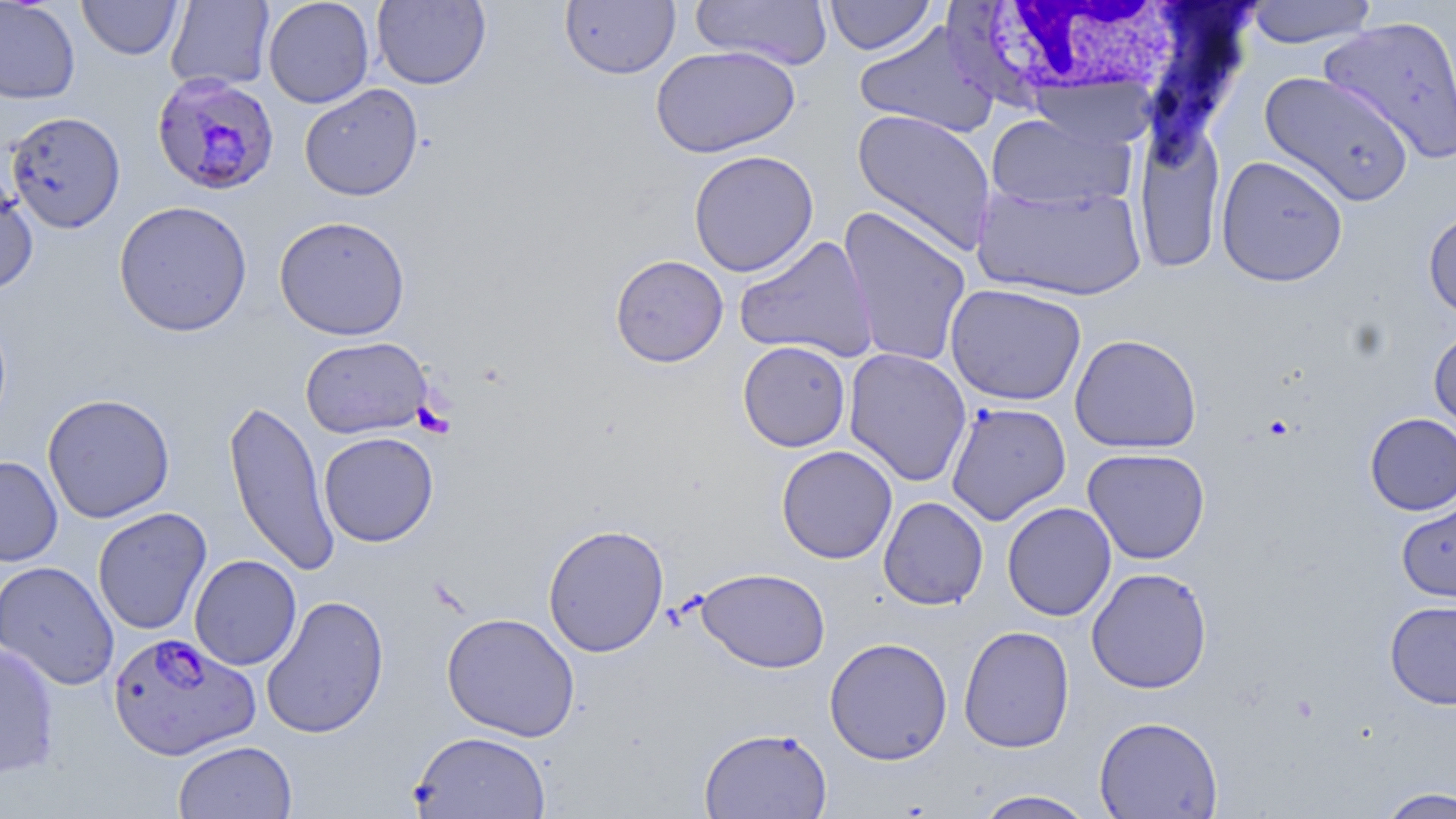
Summary:
  - Coordinate format: approximate bounding boxes as (x1, y1, x2, y2) in pixels
  - White blood cell locations: (949, 1, 1191, 107)
  - Plasmodium falciparum-infected red blood cell locations: (151, 72, 280, 196), (107, 631, 260, 761)
  - Platelet locations: (412, 403, 454, 437)
  - Uninfected red blood cell locations: (77, 0, 183, 60), (263, 0, 375, 108), (560, 0, 680, 80), (690, 0, 832, 70), (823, 0, 938, 56), (0, 1, 81, 104), (165, 1, 275, 92), (372, 1, 491, 89), (1244, 1, 1378, 48), (1319, 15, 1456, 162), (853, 20, 1000, 140), (650, 45, 801, 158), (1258, 71, 1416, 207), (299, 83, 423, 201), (851, 109, 997, 256), (5, 111, 125, 233), (985, 111, 1136, 212), (1134, 122, 1226, 275), (688, 150, 819, 277), (1216, 154, 1349, 287), (0, 171, 39, 296), (972, 181, 1148, 302), (113, 200, 253, 337), (838, 206, 973, 368), (1423, 208, 1456, 323), (274, 215, 411, 341), (734, 234, 879, 363), (609, 254, 729, 368), (944, 283, 1087, 406), (1429, 327, 1456, 440), (1069, 334, 1202, 454), (300, 336, 433, 439), (737, 340, 851, 452), (843, 347, 972, 487), (42, 393, 175, 523), (222, 397, 340, 577), (945, 401, 1072, 525), (1365, 412, 1456, 515), (318, 431, 438, 547), (776, 445, 897, 564), (1082, 447, 1210, 564), (0, 455, 63, 567), (1396, 496, 1456, 603), (878, 497, 988, 610), (1001, 502, 1117, 621), (93, 507, 212, 636), (542, 523, 670, 657), (189, 554, 302, 670), (0, 560, 119, 690), (695, 567, 831, 673), (1086, 567, 1213, 694), (261, 595, 389, 739), (1385, 600, 1456, 709), (441, 612, 581, 741), (958, 625, 1075, 753), (824, 636, 953, 765), (0, 640, 61, 780), (1094, 715, 1223, 818), (699, 727, 831, 818), (410, 730, 552, 819), (173, 740, 297, 819), (1375, 787, 1456, 818), (973, 789, 1098, 818)
  - Slide-level diagnosis: Plasmodium falciparum
  - Image size: 1456×819 pixels
  - Preparation: thin blood film
  - Magnification: 1000x
  - Field of view: single
  - Modality: optical microscopy
  - Stain: May-Grünwald-Giemsa